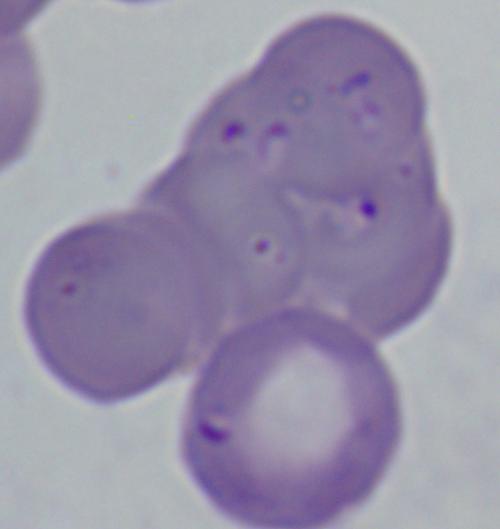
{
  "magnification": "1000x",
  "modality": "micrograph",
  "identification": "Babesia"
}